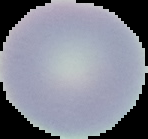

From a thin blood film. Malaria status: uninfected. Image is 148×139 pixels. Cell region segmented out of the field of view; the surrounding area is masked to black.